Locate every blood parasite and identify its species.
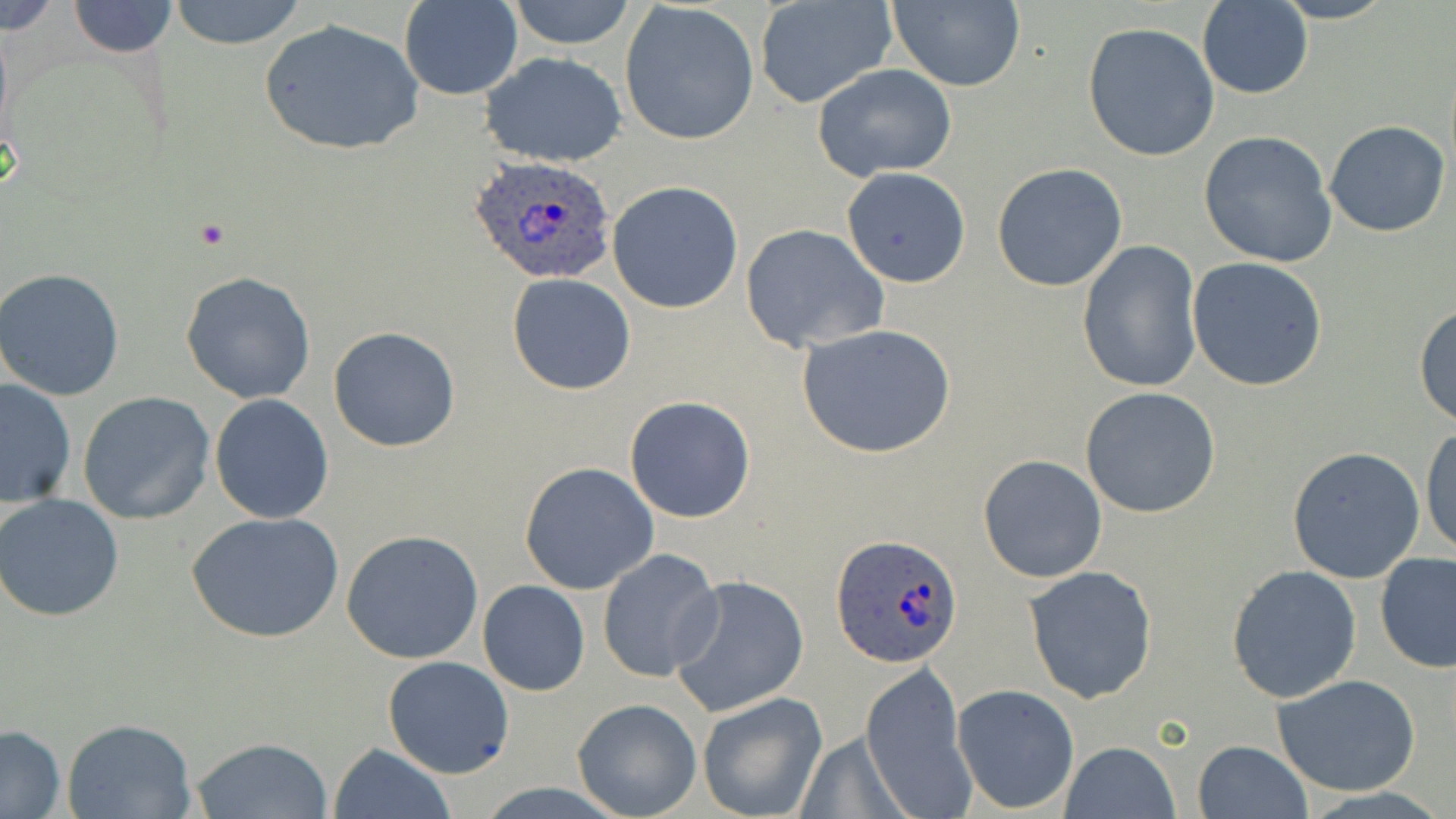
Approximate bounding boxes as (x1, y1, x2, y2) in pixels.
Plasmodium ovale-infected red blood cells: (469, 156, 617, 286), (831, 535, 962, 669).
No Plasmodium falciparum, Plasmodium malariae, Plasmodium vivax, Babesia divergens, or Trypanosoma brucei observed.

Uninfected red blood cell locations: (0, 0, 65, 36), (167, 0, 311, 50), (504, 0, 638, 49), (1269, 0, 1397, 24), (66, 1, 178, 57), (399, 1, 523, 102), (886, 1, 1025, 92), (619, 2, 761, 145), (753, 2, 897, 110), (1195, 2, 1313, 99), (259, 17, 425, 158), (1083, 23, 1219, 162), (480, 51, 627, 167), (811, 63, 957, 181), (1324, 120, 1452, 238), (1198, 129, 1338, 267), (991, 163, 1128, 292), (841, 166, 971, 286), (606, 181, 744, 313), (740, 224, 890, 353), (1077, 239, 1203, 393), (1186, 256, 1330, 392), (0, 268, 126, 401), (180, 271, 317, 404), (506, 272, 637, 394), (1414, 301, 1456, 430), (796, 323, 955, 458), (328, 325, 461, 451), (0, 376, 76, 506), (1080, 386, 1221, 519), (78, 392, 216, 523), (208, 394, 335, 524), (624, 395, 757, 523), (1420, 424, 1455, 559), (1286, 445, 1428, 582), (978, 454, 1108, 583), (519, 462, 659, 595), (0, 493, 125, 623), (186, 511, 344, 643), (341, 529, 483, 664), (597, 549, 724, 686), (1375, 552, 1456, 675), (1225, 563, 1362, 704), (1023, 566, 1158, 705), (666, 573, 809, 718), (478, 580, 589, 695), (382, 656, 514, 777), (859, 660, 977, 819), (1271, 672, 1422, 797), (951, 683, 1080, 815), (696, 691, 829, 819), (572, 698, 703, 819), (62, 718, 197, 819), (0, 725, 67, 816), (799, 733, 911, 819), (187, 735, 335, 818), (1193, 738, 1311, 818), (1060, 741, 1180, 818), (328, 743, 453, 819). Slide-level diagnosis: Plasmodium ovale. 1000x magnification. May-Grünwald-Giemsa stain. Image is 1456×819 pixels. One field of a larger specimen. Optical microscopy. Thin blood smear.